Name the blood parasite species.
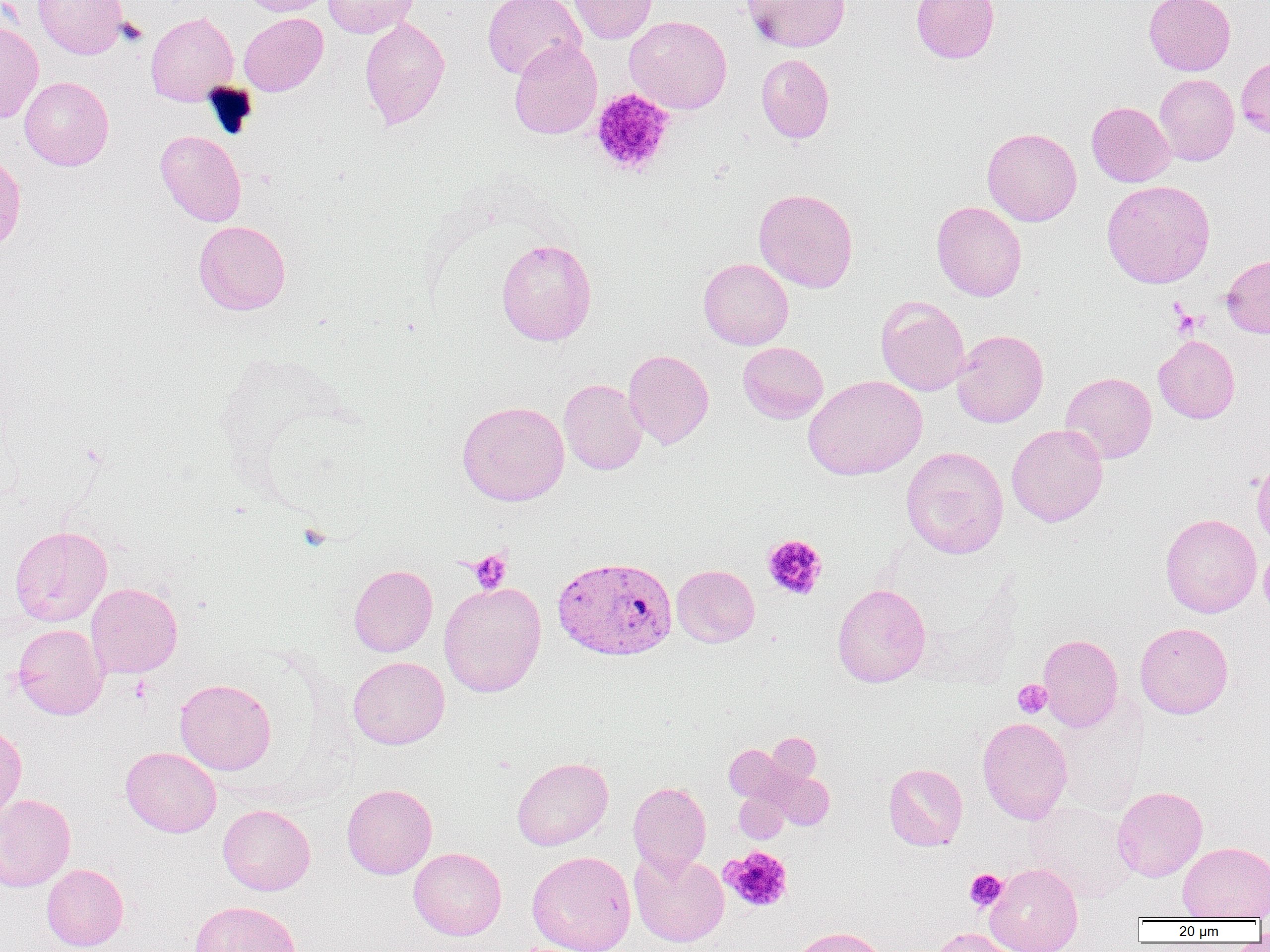

Plasmodium vivax.

Summary:
  - Coordinate format: approximate bounding boxes as named x1/y1/x2/y2 corners in pixels
  - Uninfected red blood cell locations: (x1=33, y1=0, x2=128, y2=59), (x1=239, y1=0, x2=333, y2=16), (x1=323, y1=0, x2=419, y2=38), (x1=482, y1=0, x2=586, y2=80), (x1=569, y1=0, x2=658, y2=44), (x1=742, y1=0, x2=850, y2=52), (x1=911, y1=0, x2=999, y2=63), (x1=1144, y1=0, x2=1235, y2=76), (x1=146, y1=11, x2=238, y2=105), (x1=239, y1=13, x2=328, y2=95), (x1=624, y1=15, x2=732, y2=114), (x1=359, y1=16, x2=450, y2=130), (x1=0, y1=23, x2=43, y2=123), (x1=509, y1=39, x2=602, y2=139), (x1=756, y1=53, x2=834, y2=143), (x1=1236, y1=56, x2=1270, y2=139), (x1=1154, y1=74, x2=1239, y2=166), (x1=20, y1=77, x2=114, y2=170), (x1=1086, y1=101, x2=1175, y2=187), (x1=982, y1=127, x2=1082, y2=226), (x1=155, y1=130, x2=246, y2=226), (x1=0, y1=153, x2=26, y2=258), (x1=1101, y1=179, x2=1215, y2=288), (x1=753, y1=188, x2=858, y2=293), (x1=931, y1=201, x2=1027, y2=301), (x1=193, y1=220, x2=291, y2=315), (x1=496, y1=238, x2=597, y2=346), (x1=1221, y1=253, x2=1270, y2=338), (x1=698, y1=258, x2=794, y2=349), (x1=875, y1=296, x2=970, y2=396), (x1=951, y1=329, x2=1048, y2=428), (x1=1153, y1=335, x2=1240, y2=424), (x1=738, y1=342, x2=828, y2=424), (x1=623, y1=349, x2=714, y2=449), (x1=1061, y1=372, x2=1157, y2=464), (x1=803, y1=375, x2=927, y2=481), (x1=559, y1=379, x2=647, y2=475), (x1=457, y1=401, x2=569, y2=506), (x1=1006, y1=424, x2=1108, y2=527), (x1=901, y1=446, x2=1009, y2=559), (x1=1251, y1=455, x2=1270, y2=549), (x1=1160, y1=513, x2=1262, y2=617), (x1=9, y1=525, x2=112, y2=626), (x1=1258, y1=544, x2=1270, y2=625), (x1=672, y1=564, x2=760, y2=647), (x1=348, y1=565, x2=437, y2=657), (x1=439, y1=581, x2=546, y2=697), (x1=86, y1=582, x2=183, y2=678), (x1=832, y1=583, x2=931, y2=687), (x1=1135, y1=622, x2=1233, y2=718), (x1=12, y1=623, x2=109, y2=720), (x1=1037, y1=634, x2=1123, y2=731), (x1=348, y1=656, x2=450, y2=749), (x1=174, y1=678, x2=276, y2=775), (x1=977, y1=717, x2=1073, y2=824), (x1=0, y1=724, x2=26, y2=825), (x1=768, y1=732, x2=821, y2=785), (x1=725, y1=744, x2=784, y2=801), (x1=121, y1=747, x2=221, y2=837), (x1=512, y1=757, x2=613, y2=850), (x1=883, y1=763, x2=968, y2=851), (x1=770, y1=770, x2=834, y2=830), (x1=628, y1=781, x2=711, y2=875), (x1=342, y1=784, x2=437, y2=879), (x1=1112, y1=786, x2=1207, y2=882), (x1=734, y1=790, x2=788, y2=843), (x1=0, y1=793, x2=76, y2=891), (x1=1025, y1=801, x2=1137, y2=902), (x1=218, y1=804, x2=315, y2=895), (x1=1178, y1=841, x2=1270, y2=920), (x1=409, y1=848, x2=506, y2=940), (x1=629, y1=850, x2=729, y2=947), (x1=527, y1=851, x2=636, y2=952), (x1=985, y1=862, x2=1083, y2=952), (x1=41, y1=863, x2=128, y2=951), (x1=190, y1=900, x2=301, y2=952), (x1=791, y1=926, x2=888, y2=952), (x1=926, y1=927, x2=1017, y2=952)
  - Plasmodium vivax-infected red blood cell locations: (x1=552, y1=556, x2=677, y2=661)
  - Platelet locations: (x1=589, y1=88, x2=675, y2=177), (x1=762, y1=534, x2=827, y2=600), (x1=469, y1=550, x2=512, y2=593), (x1=1013, y1=680, x2=1052, y2=718), (x1=721, y1=845, x2=794, y2=913), (x1=964, y1=868, x2=1007, y2=911)
  - Preparation: thin blood smear
  - Field of view: single
  - Magnification: 1000x
  - Modality: optical microscopy
  - Image size: 1270×952 pixels